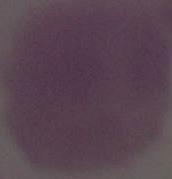

modality = micrograph
magnification = 1000x
identification = red blood cell